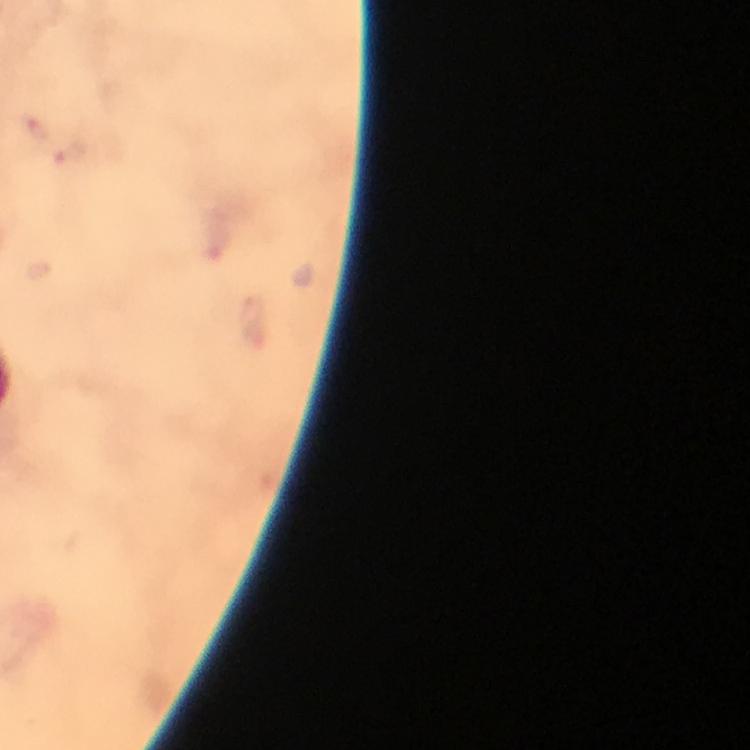

malaria_parasite_locations: 'approximate centers as (x, y) in pixels: (71, 154)'
context: from a diagnostic examination for malaria
capture: smartphone photograph through a microscope
image_size: 750×750 pixels
preparation: thick blood smear
immersion_oil: used
magnification: 100x
stain: Giemsa
cropped_from: one field of view